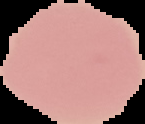
Summary:
  - Image size: 145×124 pixels
  - Image type: cell region segmented out of the field of view; surrounding area masked to black
  - Malaria status: uninfected
  - Preparation: thin blood smear